State the preparation type.
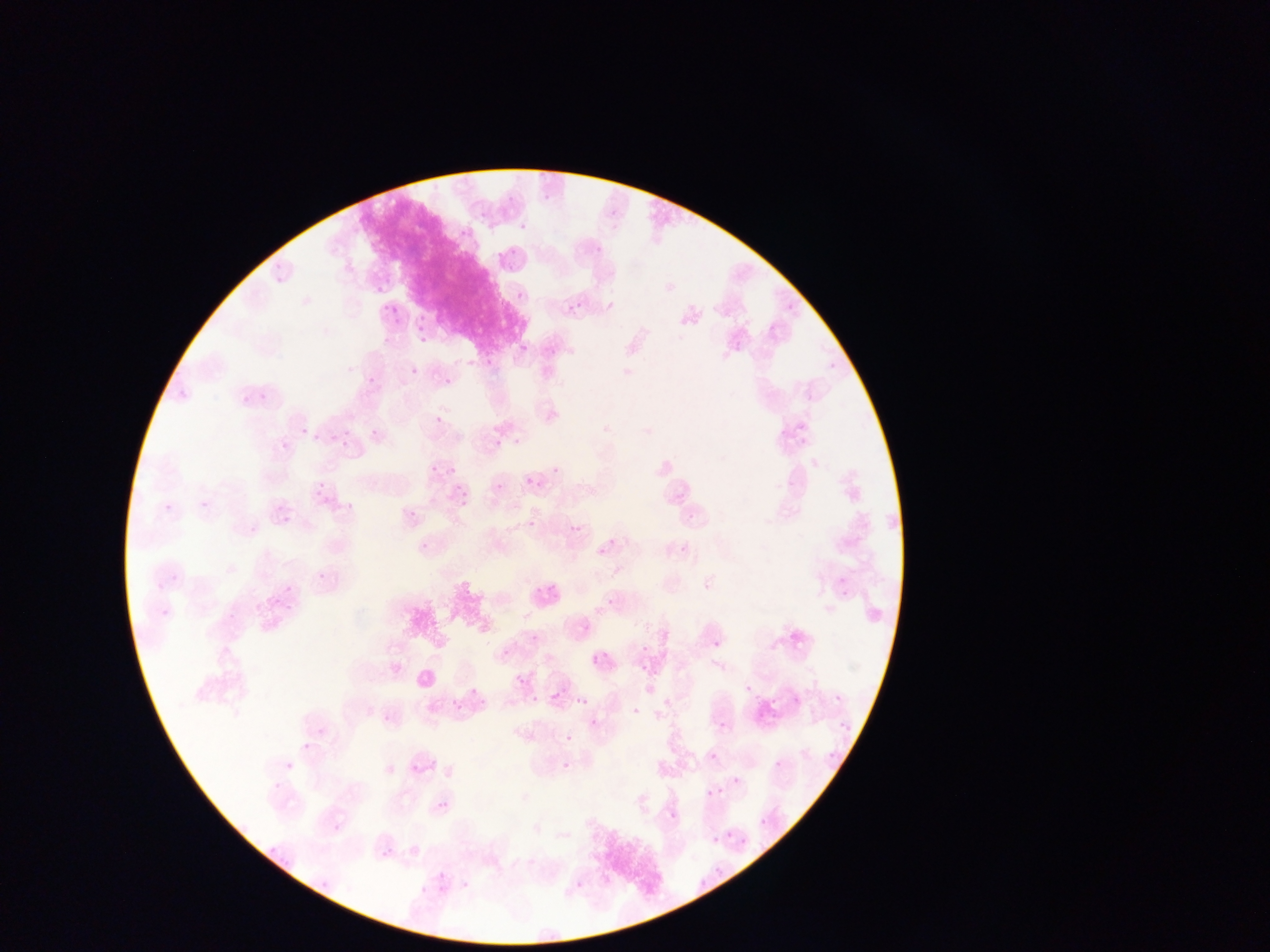

Thin blood film.

field of view = single
Plasmodium parasite locations = approximate bounding boxes as [left, top, right, bottom] in pixels: [540, 192, 555, 200], [462, 227, 471, 235], [497, 244, 519, 260], [374, 281, 391, 294], [516, 292, 524, 301], [566, 301, 582, 316], [381, 302, 396, 313], [413, 309, 427, 330], [387, 310, 406, 325], [414, 330, 436, 343], [734, 343, 742, 351], [519, 344, 528, 353], [548, 349, 556, 357], [466, 360, 474, 367], [411, 367, 420, 375], [368, 375, 379, 387], [445, 377, 453, 385], [242, 395, 249, 403], [434, 415, 442, 423], [368, 423, 385, 439], [324, 436, 332, 443], [494, 440, 502, 447], [283, 442, 290, 450], [444, 461, 457, 476], [426, 465, 436, 480], [524, 477, 532, 485], [451, 478, 465, 492], [786, 480, 792, 488], [317, 482, 324, 490], [495, 483, 503, 491], [458, 492, 473, 506], [323, 498, 331, 506], [407, 502, 416, 518], [282, 517, 290, 525], [528, 520, 536, 528], [419, 540, 435, 553], [316, 573, 324, 580], [536, 583, 555, 597], [704, 583, 711, 591], [285, 585, 293, 592], [840, 587, 849, 597], [257, 603, 266, 612], [592, 657, 600, 664], [516, 675, 525, 683], [745, 685, 753, 693], [530, 695, 538, 702], [580, 698, 588, 706], [632, 707, 639, 715], [382, 715, 390, 723], [590, 719, 598, 728], [720, 722, 728, 730], [318, 728, 326, 736], [566, 735, 572, 744], [302, 743, 309, 751], [826, 751, 838, 758], [710, 753, 718, 761], [775, 761, 782, 769], [562, 763, 570, 771], [385, 765, 394, 774], [732, 776, 741, 784], [439, 802, 447, 810], [670, 811, 677, 819], [437, 872, 445, 879], [462, 881, 469, 889] | approximate [x, y] pixel centers of objects too small to bound: [523, 227], [599, 250], [789, 307], [772, 327], [681, 336], [831, 366], [305, 432], [346, 433], [555, 470], [678, 498], [203, 503], [168, 507], [690, 517], [574, 528], [613, 542], [685, 548], [600, 553], [610, 601], [587, 628], [534, 638], [717, 645], [645, 648], [505, 654], [473, 692], [838, 698], [289, 767], [277, 786], [710, 793], [764, 822], [337, 828], [714, 839], [387, 853], [718, 869], [424, 890]
capture = mobile-phone photograph through a microscope
country = Ghana
image size = 1270×952 pixels